Locate every malaria parasite and every leukocyte.
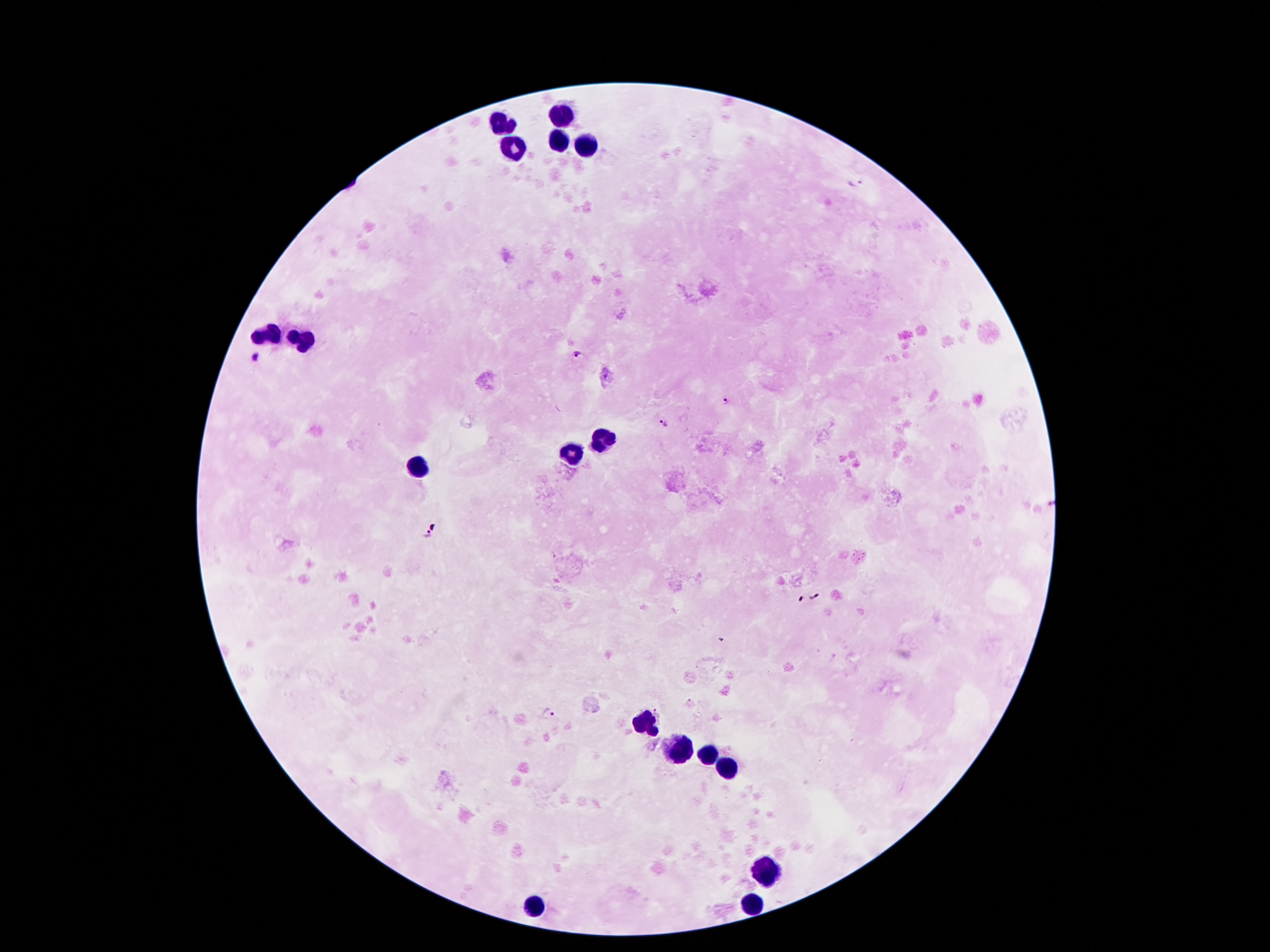

Approximate centers as (x, y) in pixels.
Malaria parasites: (857, 184), (576, 357), (258, 358), (726, 401), (663, 421), (426, 537), (815, 598), (548, 714).
Leukocytes: (560, 118), (505, 124), (560, 141), (586, 146), (516, 148), (266, 337), (304, 341), (598, 442), (573, 452), (418, 465), (646, 722), (682, 748), (706, 754), (728, 770), (770, 872), (754, 904), (536, 905).

field_of_view: one from this slide
magnification: 100x
preparation: thick blood smear
patient_malaria_status: positive for Plasmodium falciparum
capture: smartphone camera through the microscope eyepiece
image_size: 1270×952 pixels
stain: Giemsa